Report the malaria status.
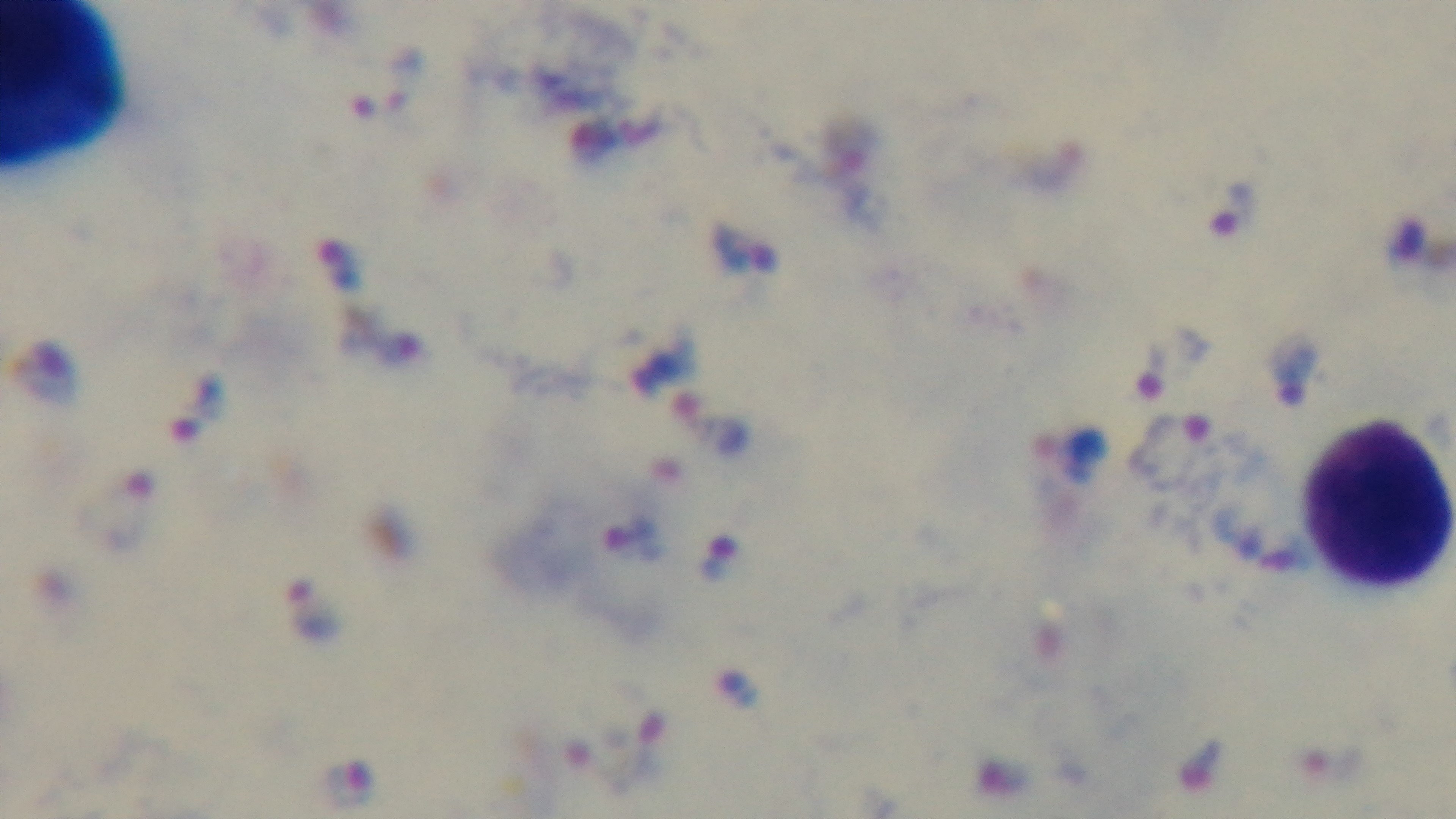
It is infected.

capture = mounted 4K digital camera
preparation = thick smear
field of view = single
stain = Giemsa
objective = 100x oil immersion
modality = light microscopy